Name the cell type shown.
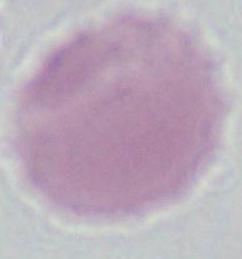

An erythrocyte.

Summary:
  - Magnification: 1000x
  - Modality: photomicrograph